Outline each Plasmodium ovale-infected red blood cell.
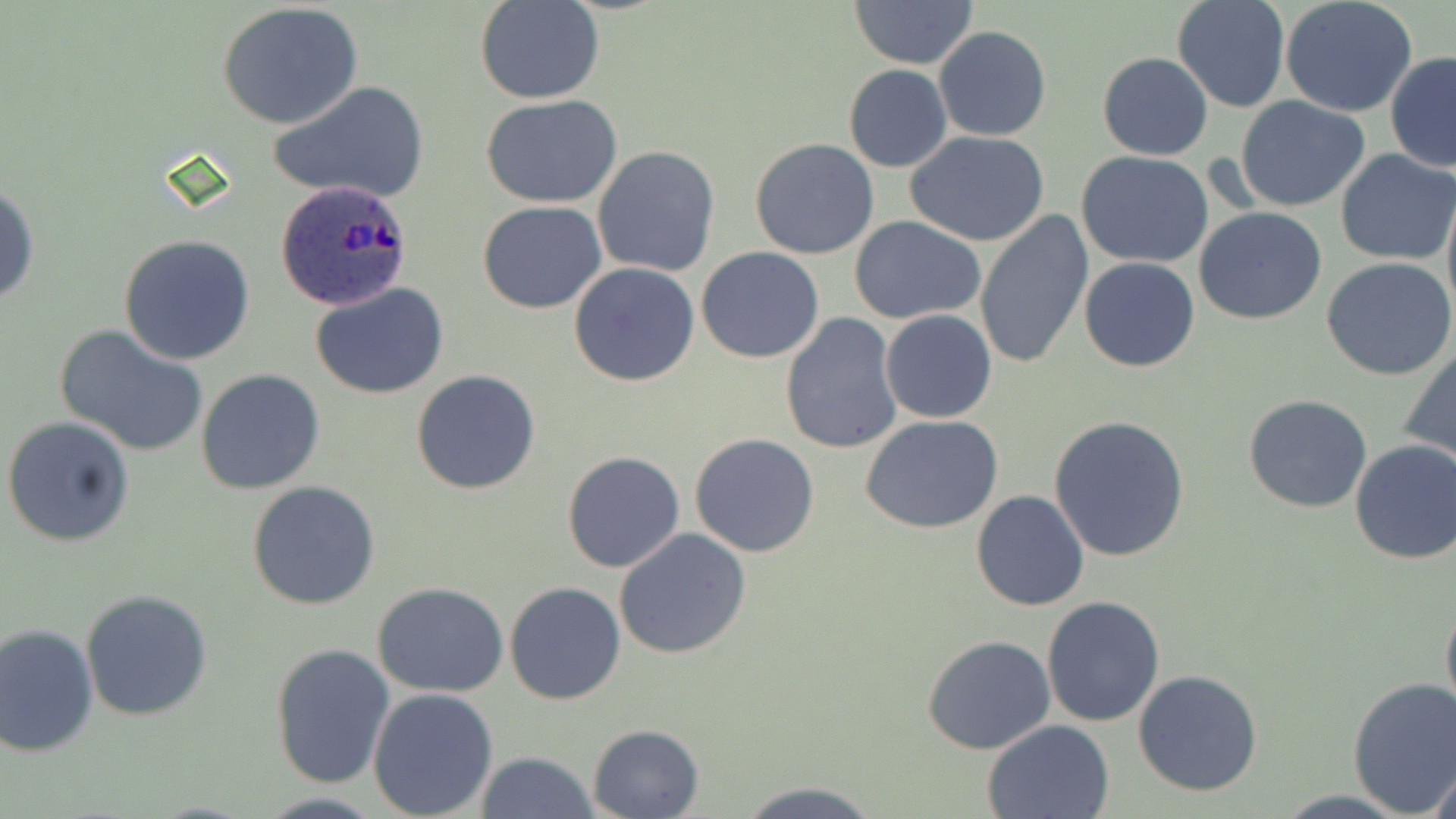

Approximate bounding boxes as [x1, y1, x2, y2] in pixels.
Plasmodium ovale-infected red blood cells: [274, 182, 413, 310].

slide-level diagnosis = Plasmodium ovale
uninfected red blood cell locations = approximate bounding boxes as [x1, y1, x2, y2] in pixels: [474, 0, 605, 104], [849, 0, 979, 68], [1171, 0, 1290, 112], [1280, 0, 1418, 117], [216, 3, 365, 129], [933, 26, 1053, 143], [1097, 51, 1213, 161], [1386, 52, 1456, 173], [843, 64, 951, 173], [270, 82, 429, 206], [480, 94, 627, 206], [1234, 96, 1371, 211], [904, 129, 1050, 245], [750, 137, 878, 259], [592, 145, 721, 278], [1076, 150, 1214, 269], [1335, 150, 1455, 263], [1, 180, 39, 311], [1441, 185, 1456, 329], [477, 201, 606, 315], [1194, 207, 1327, 324], [973, 211, 1093, 371], [850, 217, 988, 323], [118, 234, 255, 365], [696, 247, 825, 363], [571, 255, 826, 375], [1079, 257, 1200, 372], [1322, 257, 1456, 382], [569, 263, 699, 386], [312, 284, 449, 400], [880, 309, 997, 423], [780, 311, 903, 454], [57, 326, 210, 457], [1401, 343, 1456, 467], [196, 369, 325, 495], [411, 370, 542, 495], [1242, 394, 1373, 513], [2, 415, 135, 548], [1047, 415, 1191, 562], [862, 417, 1005, 534], [690, 433, 820, 557], [1348, 439, 1456, 565], [561, 451, 686, 573], [248, 480, 381, 611], [970, 490, 1090, 611], [613, 529, 753, 661], [504, 581, 628, 704], [372, 583, 511, 698], [80, 590, 214, 722], [1440, 593, 1456, 728], [1041, 596, 1166, 726], [0, 623, 100, 757], [922, 636, 1057, 755], [269, 641, 396, 790], [1132, 670, 1263, 797], [1347, 675, 1456, 816], [367, 687, 498, 819], [982, 719, 1115, 818], [587, 724, 704, 818], [474, 751, 596, 819], [1427, 756, 1455, 818], [739, 781, 881, 818]
modality = light microscopy
preparation = thin blood smear
stain = May-Grünwald-Giemsa
image size = 1456×819 pixels
magnification = 1000x
field of view = one of a larger specimen